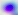 400x magnification. Micrograph. Toxoplasma gondii is shown.